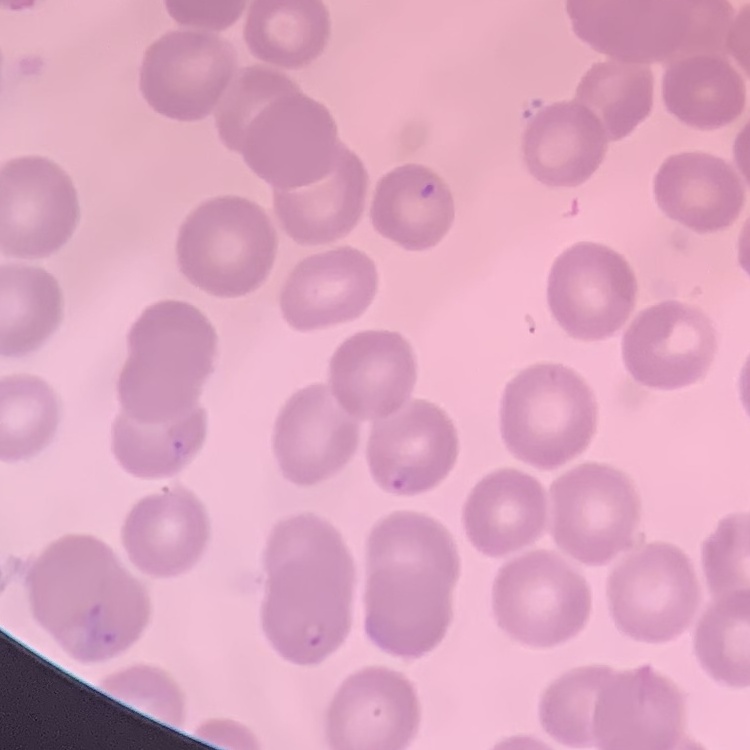
The red blood cells show no rouleaux formation. Stained with either Field's or Giemsa. Thin blood film. One tile cut from a larger photomicrograph.